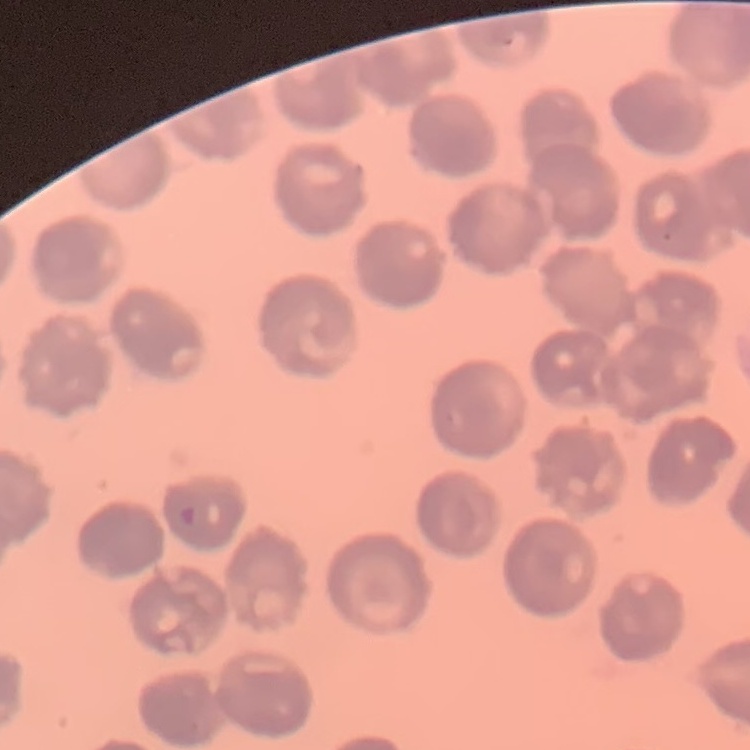
erythrocyte morphology = no rouleaux formation
preparation = thin blood film
stain = Field's or Giemsa
image type = square crop of a larger photomicrograph